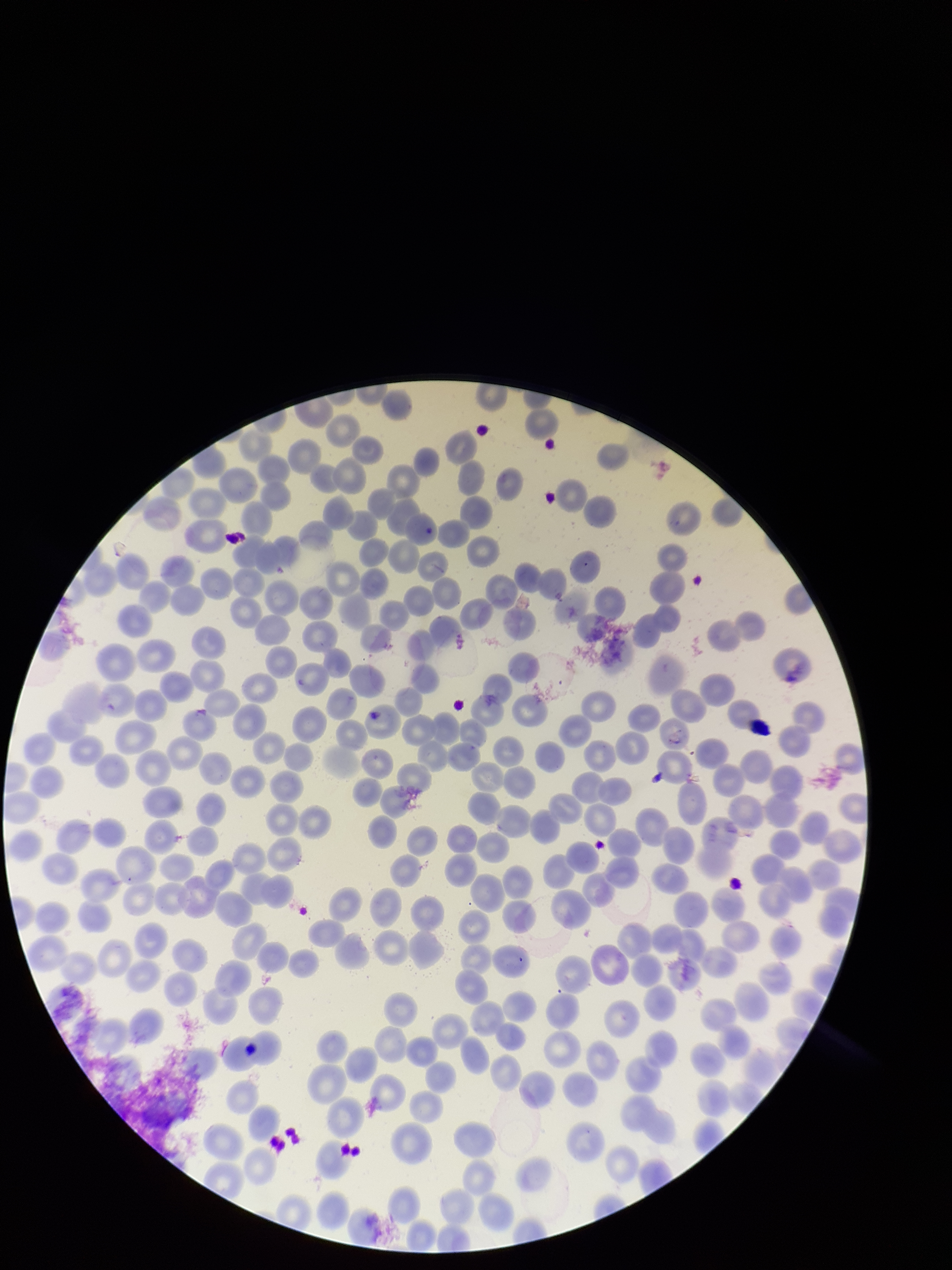
parasitized red blood cell count = 0
patient malaria status = infected
parasitized red blood cells = none seen
stain = Giemsa
red blood cell count = 286
field of view = one from this slide
preparation = thin blood smear
species reported for this patient = Plasmodium vivax
image size = 952×1270 pixels
capture = smartphone photograph through the microscope eyepiece